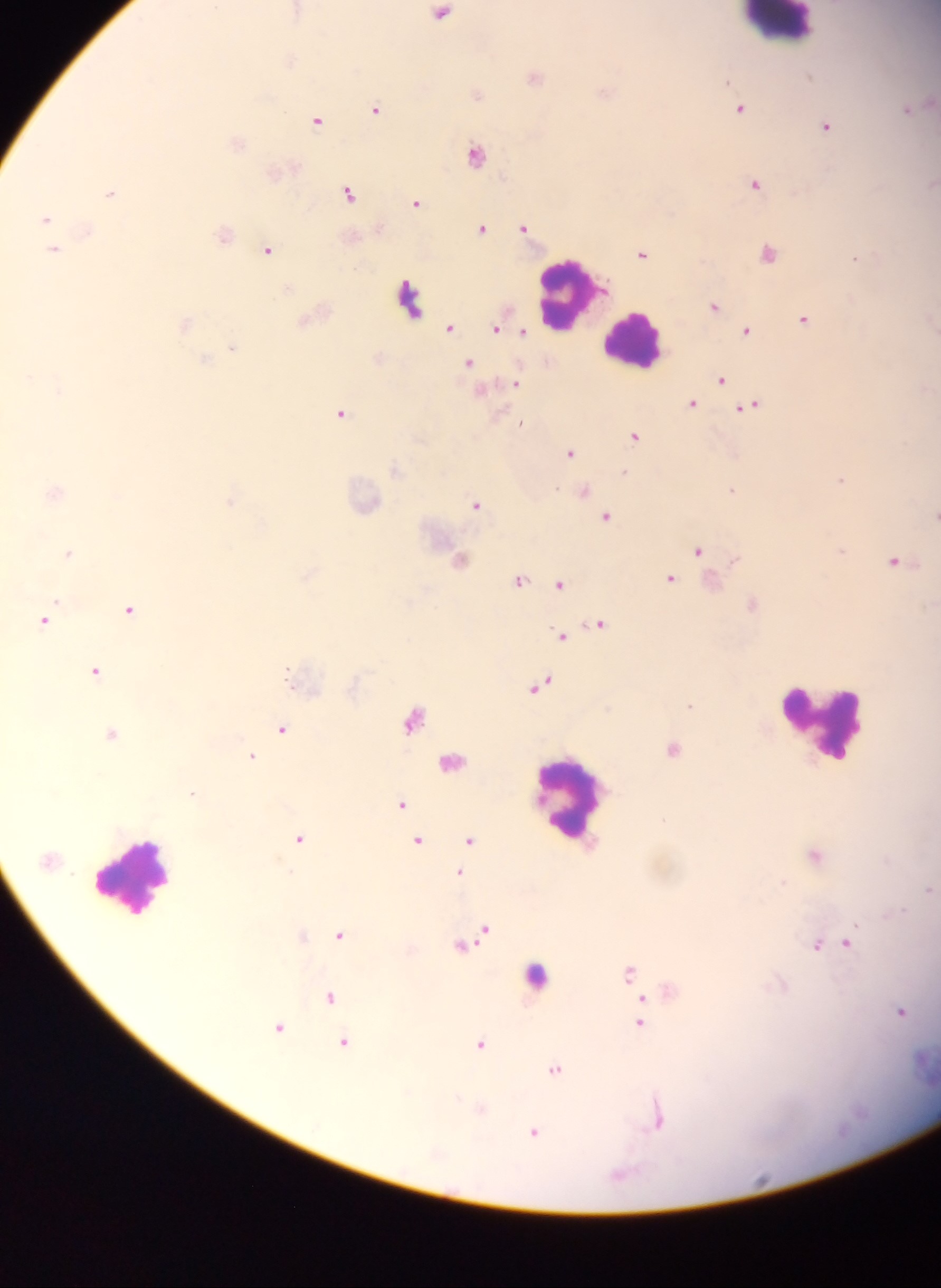

Approximate centers as x y in pixels. Plasmodium parasite locations: 442 14; 726 81; 377 108; 740 109; 907 110; 317 121; 826 125; 475 154; 754 184; 110 194; 348 194; 415 202; 45 220; 481 229; 523 230; 224 234; 55 250; 269 250; 768 253; 641 254; 855 259; 712 308; 803 318; 449 329; 746 331; 721 380; 341 413; 634 437; 571 453; 841 479; 732 490; 584 491; 231 503; 476 506; 606 518; 840 549; 698 552; 68 553; 733 561; 895 562; 308 575; 669 577; 520 581; 559 585; 57 603; 128 608; 45 621; 595 626; 561 637; 94 670; 288 671; 543 684; 690 705; 412 719; 281 729; 111 732; 672 749; 251 756; 191 794; 401 804; 300 838; 470 840; 418 841; 816 854; 458 874; 782 881; 926 891; 903 909; 884 915; 855 924; 483 928; 477 932; 338 935; 465 944; 847 944; 816 945; 628 971; 330 994; 642 998; 900 1011; 638 1023; 279 1027; 343 1042; 480 1042; 555 1069; 655 1127; 533 1132. Leukocyte locations: 776 22; 405 293; 569 300; 634 334; 824 724; 565 805; 132 871. Mobile-phone photograph taken through the microscope. Image is 941×1288 pixels. Sample from Ghana. Thick blood smear. Single field of view.